Assess this cell for malaria.
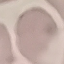

Uninfected.

Giemsa stain. Automatically extracted cell patch, resized to 64 × 64 pixels. Acquired by smartphone through the microscope eyepiece. Thin blood film.